Give the position of every Plasmodium parasite visible.
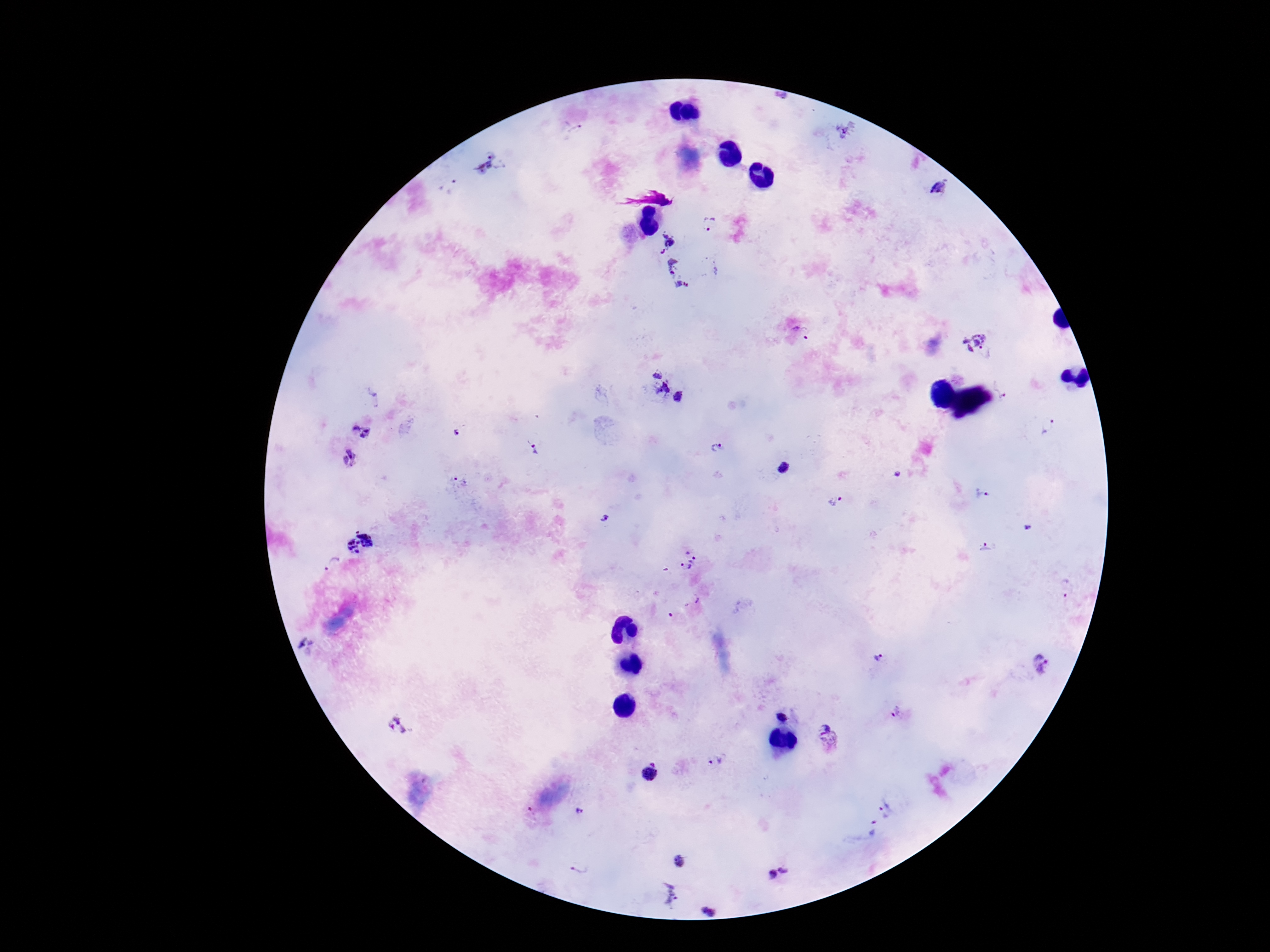
Approximate object centers, in pixels from the top-left corner.
Plasmodium parasites: (x=782, y=98), (x=574, y=128), (x=846, y=129), (x=489, y=165), (x=449, y=187), (x=940, y=189), (x=710, y=224), (x=664, y=241), (x=674, y=268), (x=682, y=291), (x=806, y=333), (x=975, y=341), (x=666, y=386), (x=1002, y=388), (x=1049, y=427), (x=361, y=432), (x=532, y=448), (x=715, y=448), (x=351, y=458), (x=786, y=467), (x=461, y=482), (x=983, y=495), (x=837, y=502), (x=606, y=518), (x=359, y=542), (x=986, y=549), (x=687, y=560), (x=331, y=564), (x=1066, y=587), (x=878, y=657), (x=1042, y=666), (x=896, y=712), (x=784, y=717), (x=399, y=724), (x=827, y=738), (x=716, y=761), (x=649, y=772), (x=888, y=810), (x=579, y=811), (x=531, y=813), (x=871, y=829), (x=680, y=860), (x=580, y=867), (x=779, y=872), (x=670, y=893), (x=710, y=910).

patient malaria status = infected
stain = Giemsa
field of view = one from this slide
image size = 1270×952 pixels
preparation = thick blood smear
capture = smartphone camera through the microscope eyepiece
magnification = 100x